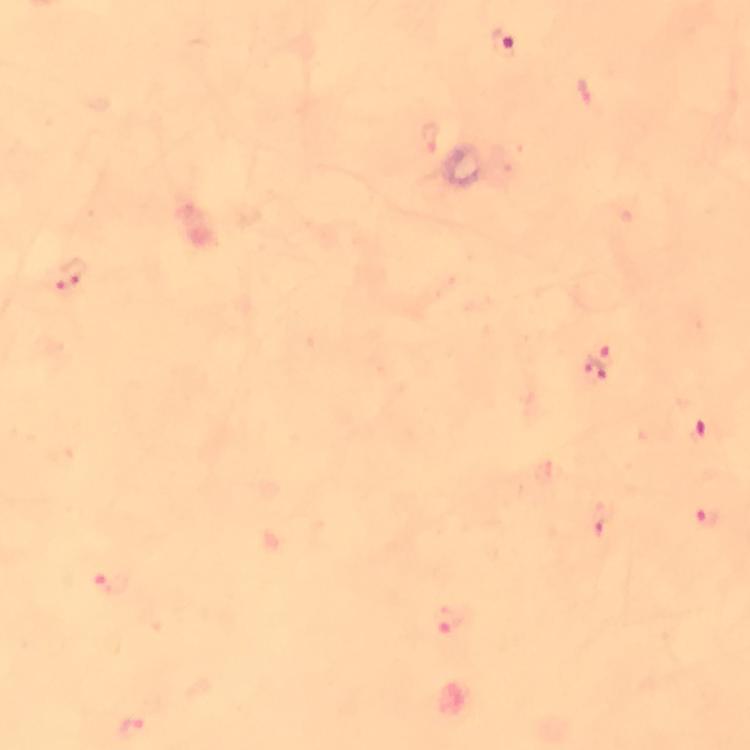
context = from a diagnostic examination for malaria
preparation = thick blood smear
image size = 750×750 pixels
magnification = 100x
Plasmodium parasite locations = approximate centers as {x, y} in pixels: {505, 44}, {72, 277}, {603, 357}, {593, 373}, {703, 435}, {705, 519}, {602, 521}, {111, 581}, {452, 621}, {132, 730}
capture = smartphone mounted on the microscope
cropped from = one field of view
stain = Giemsa
immersion oil = used